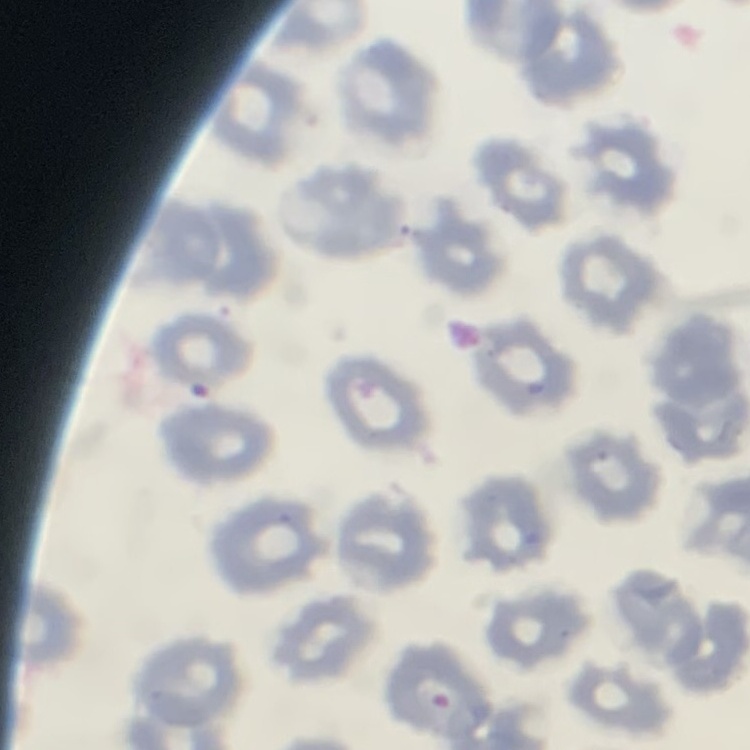
Summary:
  - Red blood cell morphology: no rouleaux formation
  - Stain: Field's or Giemsa
  - Image type: one tile cut from a larger photomicrograph
  - Preparation: thin peripheral smear